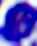 A white blood cell is seen. Photomicrograph. 400x magnification.